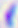
Summary:
  - Magnification: 400x
  - Modality: photomicrograph
  - Identification: Toxoplasma gondii